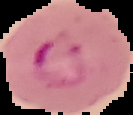

preparation = thin blood film
result = Plasmodium parasites identified
image size = 133×115 pixels
image type = segmented cell region on a black background